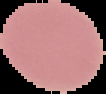

preparation: thin blood smear
result: no Plasmodium parasites detected
image_type: cell region segmented out of the field of view; surrounding area masked to black
image_size: 106×94 pixels